Assess the morphology of the erythrocytes.
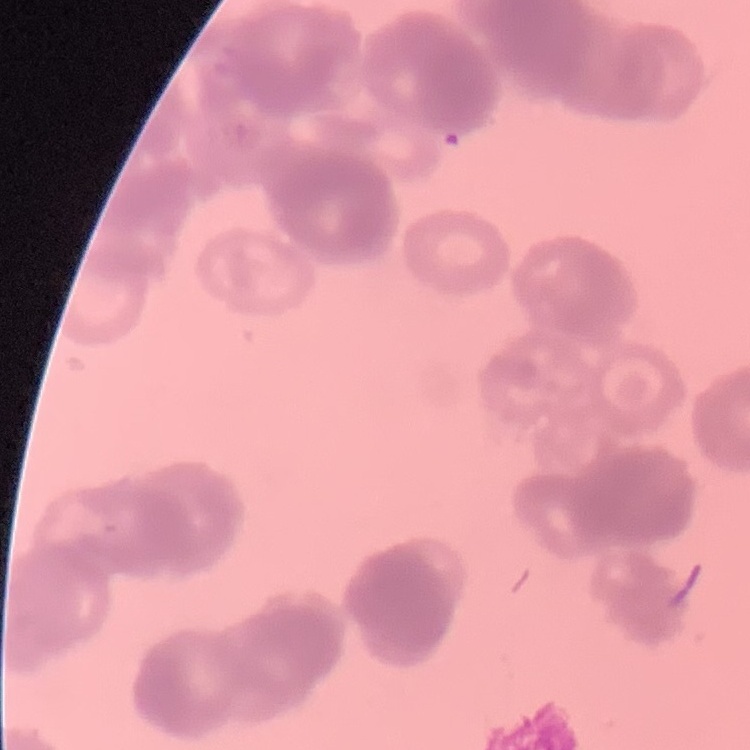

Rouleaux formation.

One tile cut from a larger photomicrograph. Thin blood film. Field's or Giemsa stain.